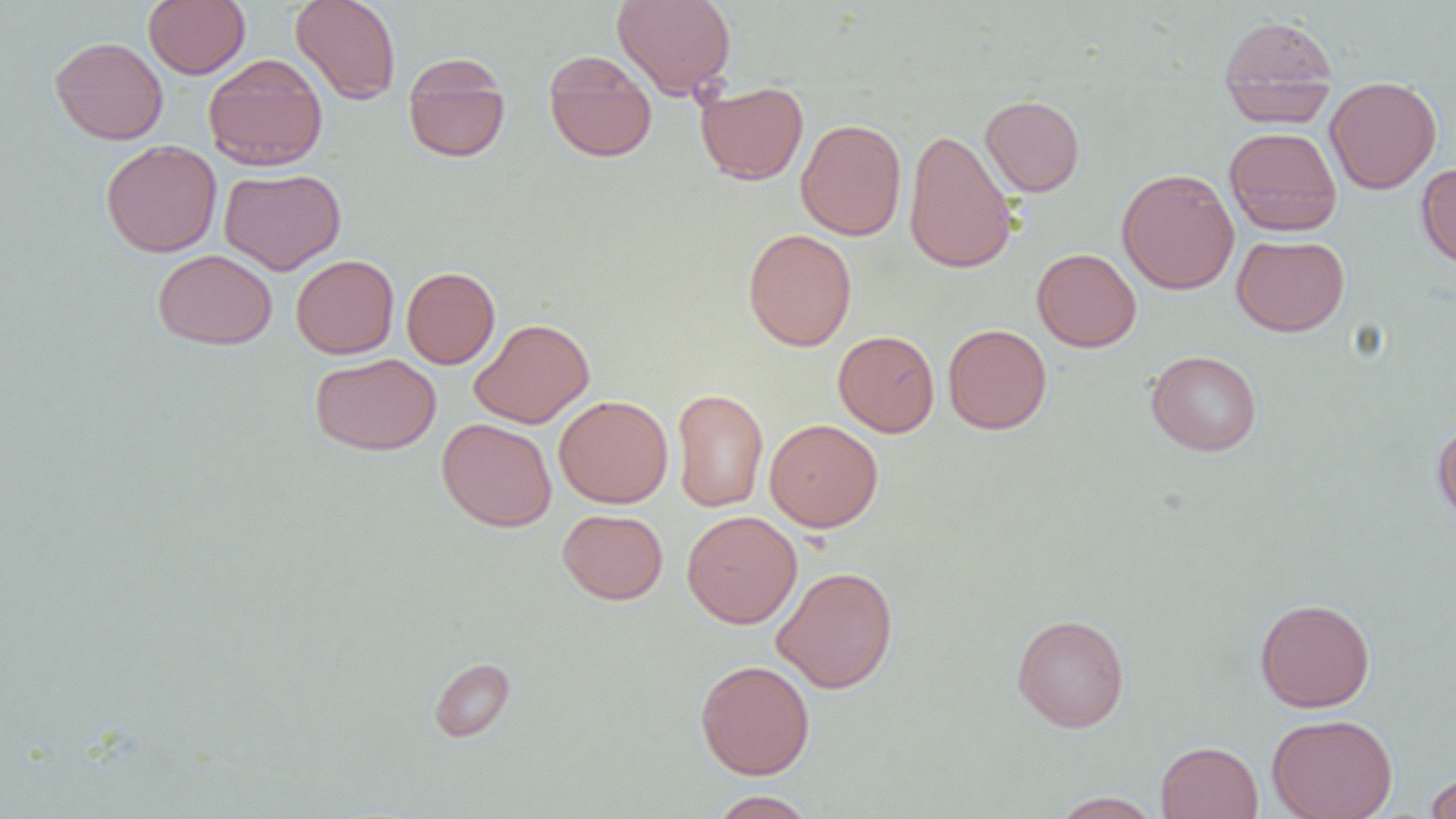
Summary:
  - Coordinate format: approximate bounding boxes as (x1, y1, x2, y2) in pixels
  - Uninfected red blood cell locations: (290, 0, 401, 104), (612, 0, 736, 99), (143, 1, 250, 78), (1219, 14, 1339, 126), (50, 36, 168, 145), (544, 52, 657, 163), (203, 54, 328, 171), (403, 54, 510, 163), (1326, 76, 1442, 194), (695, 81, 808, 185), (980, 95, 1085, 197), (795, 118, 906, 241), (1224, 127, 1342, 236), (903, 129, 1017, 275), (100, 140, 222, 257), (1417, 163, 1456, 271), (219, 167, 345, 274), (1116, 168, 1240, 295), (742, 228, 857, 351), (1232, 234, 1350, 336), (1032, 248, 1141, 352), (152, 249, 277, 350), (290, 254, 399, 359), (401, 266, 500, 369), (469, 318, 594, 428), (943, 324, 1052, 434), (833, 330, 939, 437), (1147, 350, 1262, 456), (310, 353, 440, 455), (671, 388, 769, 512), (554, 395, 673, 508), (437, 417, 556, 532), (764, 418, 883, 532), (1432, 419, 1456, 529), (557, 509, 668, 604), (682, 510, 803, 629), (772, 565, 898, 694), (1255, 597, 1376, 712), (1012, 613, 1129, 732), (429, 657, 515, 742), (695, 659, 815, 779), (1267, 713, 1397, 819), (1155, 741, 1263, 818), (1424, 771, 1456, 819), (708, 790, 818, 818), (1049, 791, 1164, 818)
  - Slide-level diagnosis: negative for blood parasites
  - Preparation: thin blood film
  - Image size: 1456×819 pixels
  - Modality: light microscopy
  - Magnification: 1000x
  - Field of view: one of a larger specimen